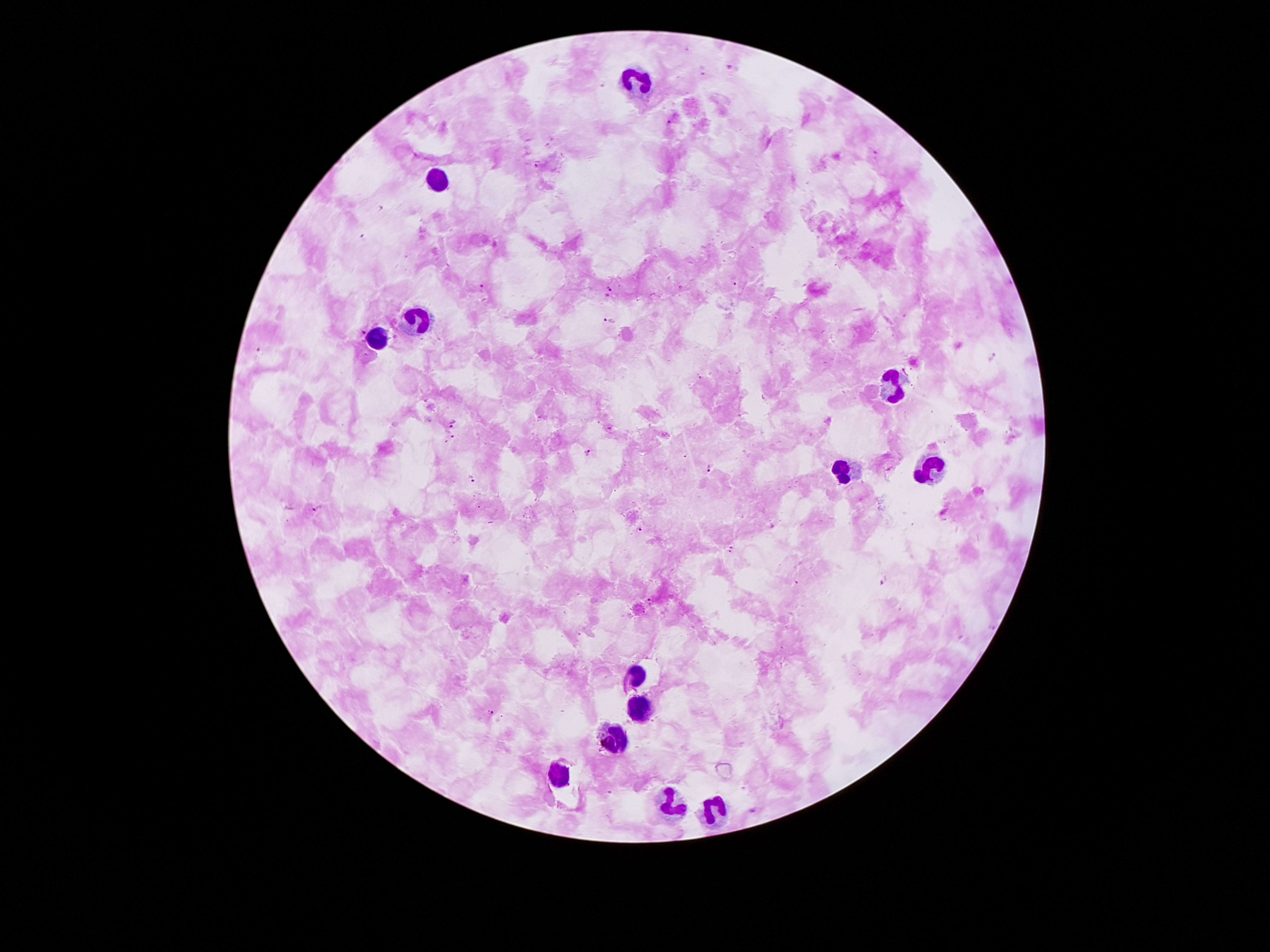
{
  "capture": "smartphone through the microscope eyepiece",
  "field_of_view": "one from this slide",
  "leukocyte_locations": "approximate centers as (x, y) in pixels: (635, 77), (435, 179), (415, 315), (378, 339), (897, 385), (932, 468), (840, 471), (635, 670), (640, 711), (615, 737), (561, 775), (662, 805), (714, 810)",
  "patient_malaria_status": "infected with Plasmodium falciparum",
  "image_size": "1270×952 pixels",
  "malaria_parasite_locations": "approximate centers as (x, y) in pixels: (731, 65), (704, 71), (668, 121), (875, 152), (536, 164), (737, 281), (483, 286), (611, 289), (610, 319), (363, 332), (995, 356), (454, 425), (449, 434), (588, 451), (711, 469), (471, 478), (317, 509), (639, 530), (730, 548), (886, 584), (652, 597), (491, 711)",
  "magnification": "100x",
  "stain": "Giemsa",
  "preparation": "thick peripheral-blood smear"
}